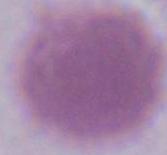
Captured at 1000x magnification. Photomicrograph. A red blood cell is seen.